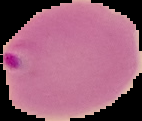

Segmented cell region on a black background. From a thin blood film. Image is 142×121 pixels. Malaria status: parasitized.